Assess this cell for malaria.
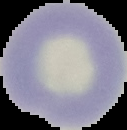

Uninfected.

Image is 127×130 pixels. Segmented cell region on a black background. From a thin blood film.